Name the parasite shown.
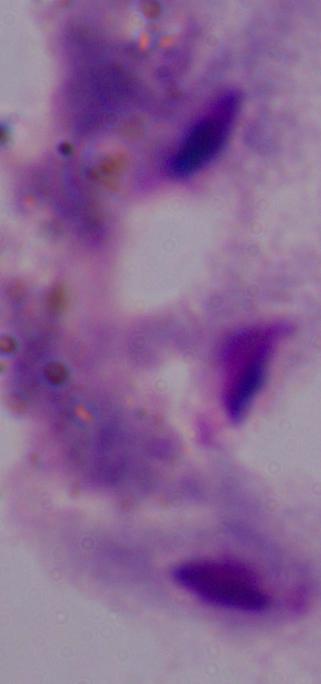
A trichomonad.

1000x magnification. Photomicrograph.